Give the position of every leukocyte visible.
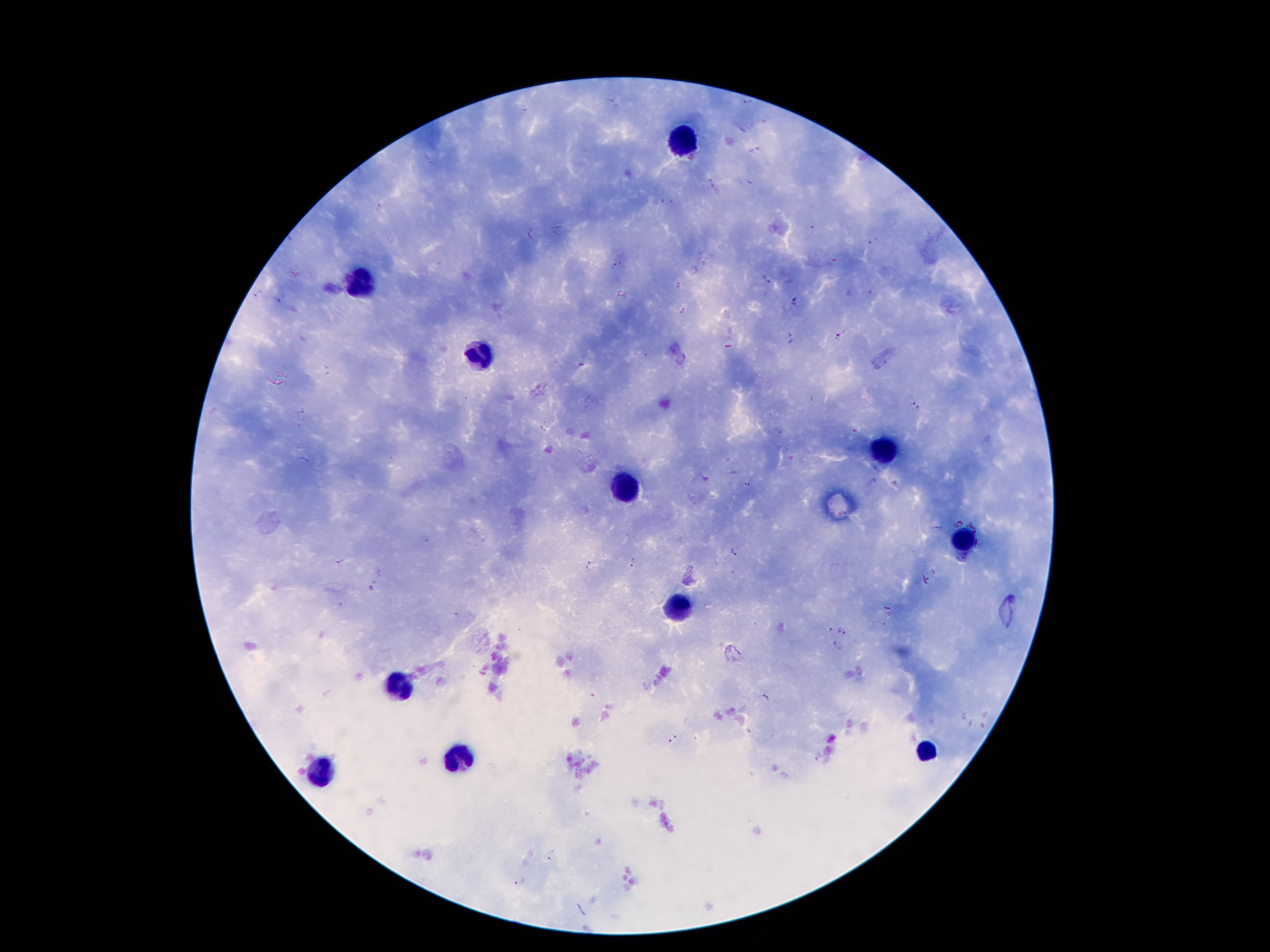
Approximate centers as {x, y} in pixels.
Leukocytes: {678, 141}, {365, 284}, {476, 353}, {889, 454}, {629, 489}, {965, 538}, {677, 608}, {399, 684}, {923, 749}, {460, 758}, {319, 772}.

Summary:
  - Plasmodium parasite locations: {610, 98}, {749, 103}, {525, 108}, {764, 121}, {755, 148}, {710, 183}, {746, 183}, {666, 201}, {380, 207}, {810, 224}, {531, 234}, {876, 240}, {617, 263}, {768, 278}, {870, 292}, {257, 294}, {277, 300}, {795, 300}, {838, 336}, {792, 337}, {645, 355}, {580, 364}, {327, 371}, {915, 406}, {300, 410}, {304, 417}, {297, 425}, {541, 429}, {304, 461}, {876, 469}, {872, 481}, {746, 485}, {958, 524}, {974, 524}, {935, 527}, {427, 540}, {733, 551}, {339, 560}, {588, 565}, {630, 565}, {829, 632}, {841, 632}, {837, 647}, {763, 697}, {673, 739}, {552, 855}, {518, 882}
  - Field of view: single
  - Magnification: 100x
  - Patient malaria status: infected with Plasmodium falciparum
  - Stain: Giemsa
  - Image size: 1270×952 pixels
  - Capture: smartphone through the microscope eyepiece
  - Preparation: thick peripheral-blood smear